Comment on the morphology of the erythrocytes.
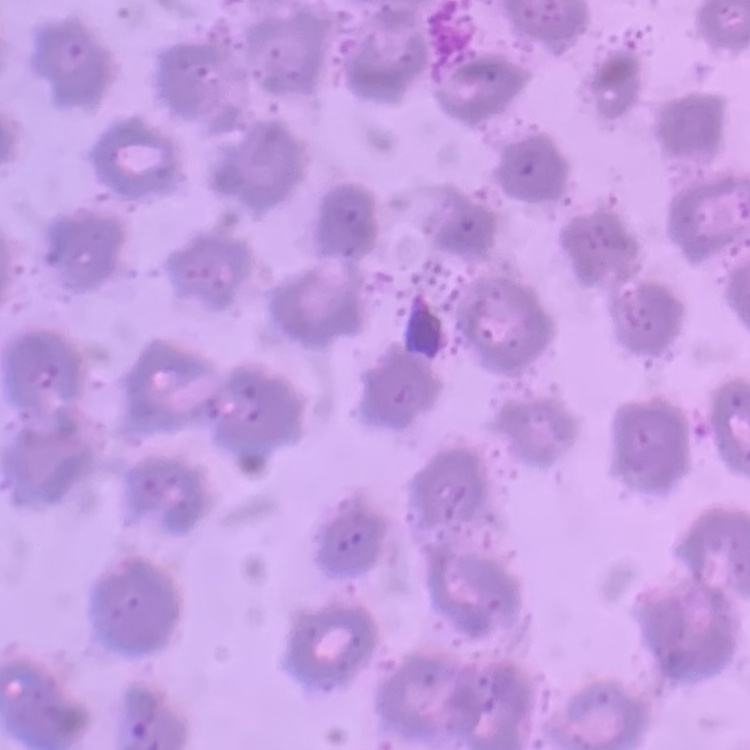

No rouleaux formation.

Summary:
  - Preparation: thin blood smear
  - Stain: Field's or Giemsa
  - Image type: one tile cut from a larger photomicrograph